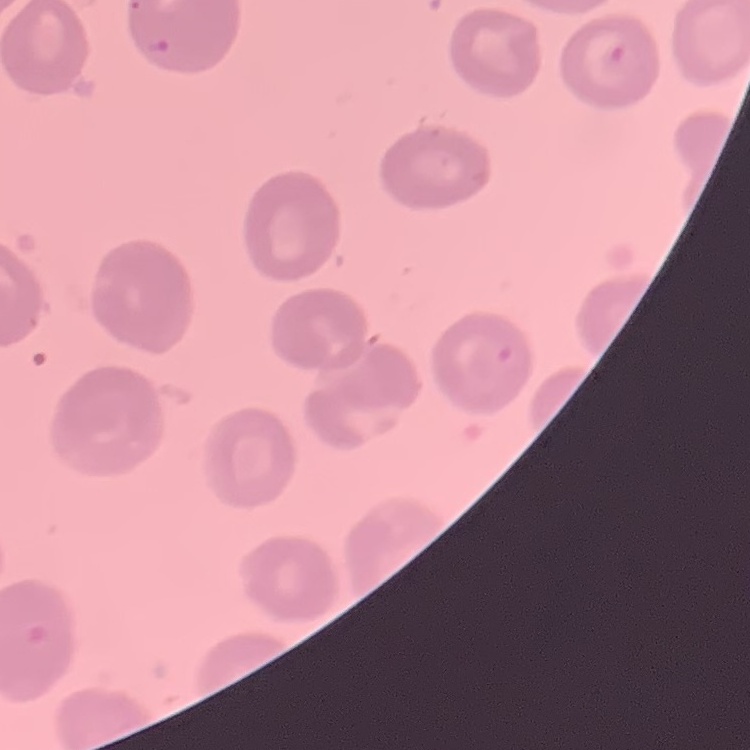

The red blood cells show no rouleaux formation. Thin peripheral smear. Stained with either Field's or Giemsa. Square crop of a larger photomicrograph.